Point out each Plasmodium parasite.
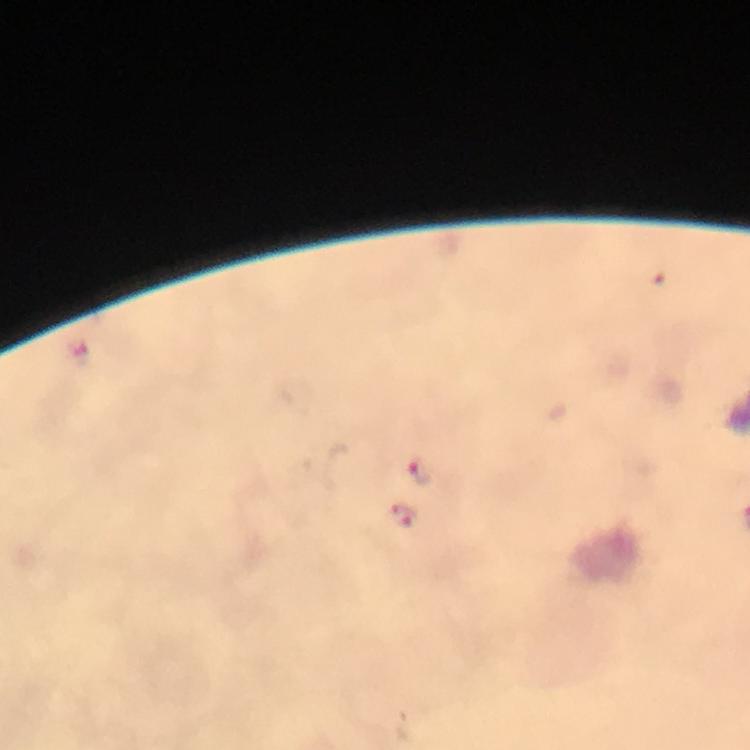
Approximate centers as (x, y) in pixels.
Plasmodium parasites: (662, 278), (79, 353), (418, 470), (404, 515).

context = from a malaria diagnostic workup
image size = 750×750 pixels
preparation = thick smear
stain = Giemsa
capture = smartphone photograph through a microscope
cropped from = one field of view
magnification = 100x
immersion oil = applied